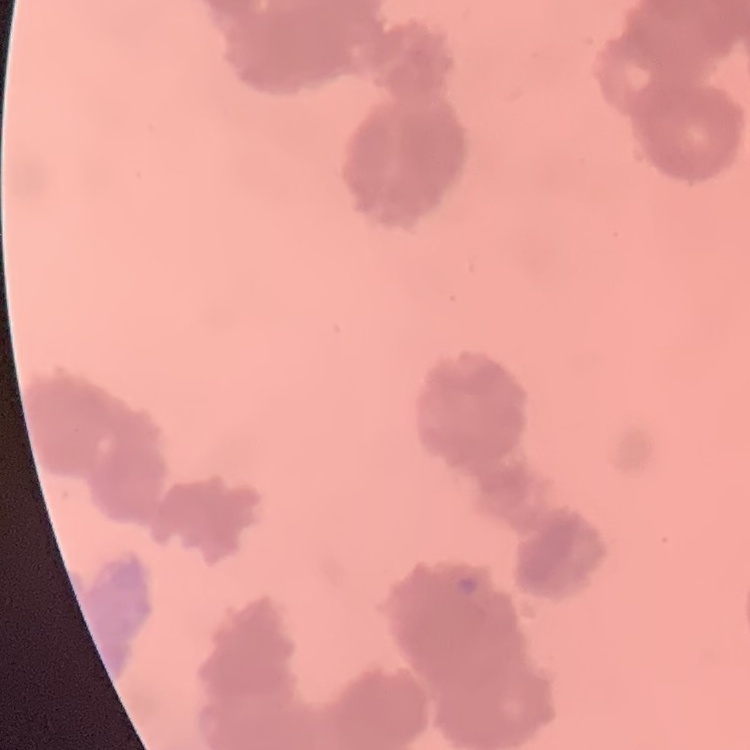 The red blood cells exhibit rouleaux formation. Field's or Giemsa stain. Square crop of a larger photomicrograph. Thin blood smear.